Locate and identify every blood parasite.
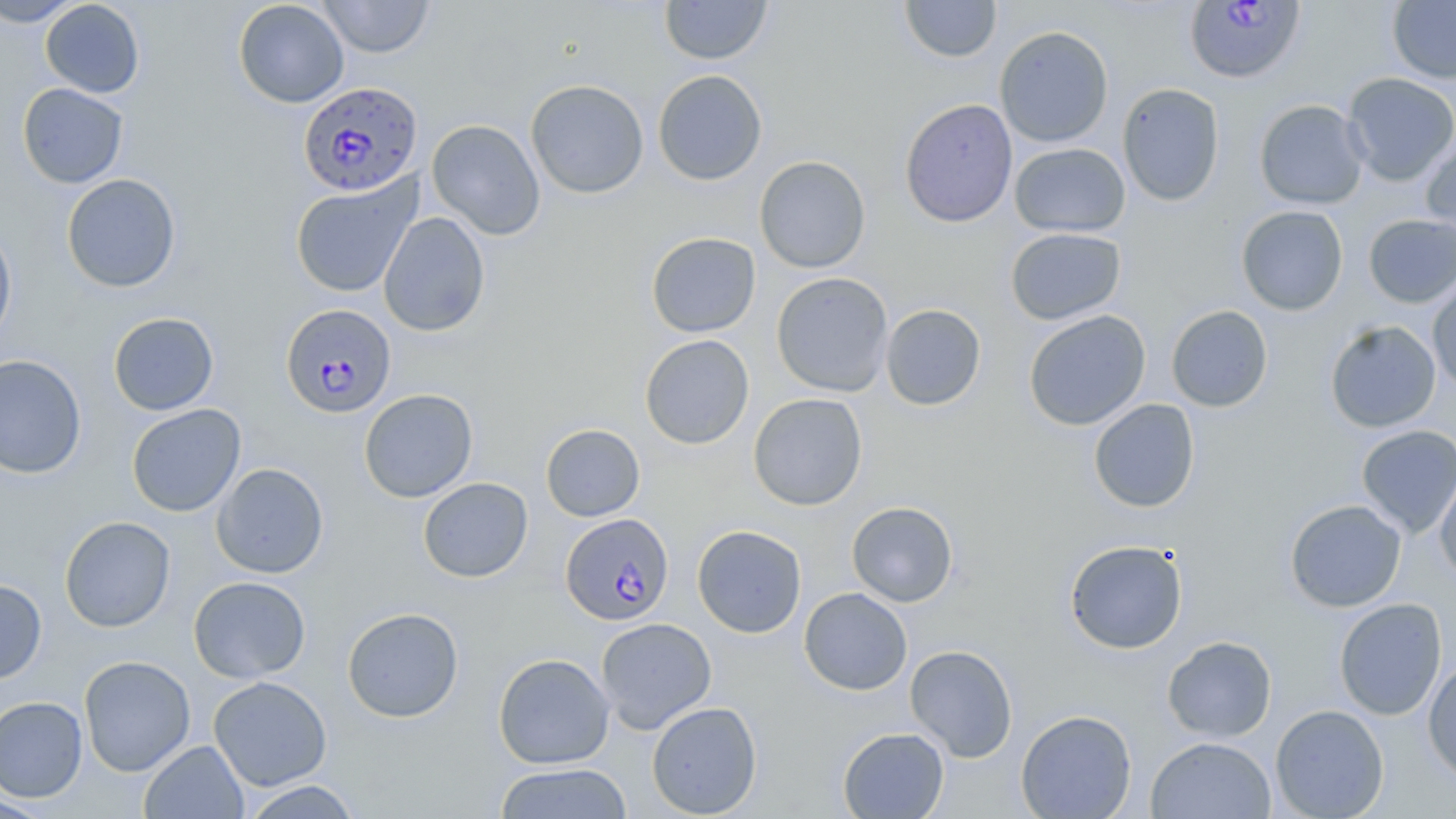

Approximate bounding boxes as (x1,y1)-(x2,y2) corner pairs in pixels.
Plasmodium falciparum-infected red blood cells: (1184,0)-(1305,84), (298,81)-(423,196), (282,303)-(398,418), (560,513)-(674,626).
No Plasmodium ovale, Plasmodium malariae, Plasmodium vivax, Babesia divergens, or Trypanosoma brucei observed.

{
  "slide_level_diagnosis": "Plasmodium falciparum",
  "preparation": "thin blood smear",
  "modality": "light microscopy",
  "magnification": "1000x",
  "image_size": "1456×819 pixels",
  "field_of_view": "single",
  "uninfected_red_blood_cell_locations": "approximate bounding boxes as (x1,y1)-(x2,y2) corner pairs in pixels: (0,0)-(83,27), (40,0)-(145,98), (233,0)-(349,108), (317,0)-(434,58), (660,0)-(772,65), (900,1)-(1001,63), (1388,1)-(1456,84), (995,26)-(1114,147), (652,69)-(768,186), (1341,72)-(1456,186), (525,79)-(649,198), (1117,82)-(1225,207), (17,83)-(128,188), (900,98)-(1018,228), (1254,99)-(1369,209), (427,119)-(545,240), (1421,135)-(1456,246), (1010,143)-(1130,237), (755,155)-(871,274), (61,173)-(181,293), (290,176)-(421,297), (1236,205)-(1348,315), (378,212)-(490,337), (1363,214)-(1456,308), (0,221)-(17,350), (1005,227)-(1126,325), (646,232)-(761,337), (771,272)-(894,397), (1427,276)-(1456,393), (880,304)-(986,411), (1166,305)-(1273,412), (1023,310)-(1151,431), (108,312)-(219,416), (1325,320)-(1441,433), (639,334)-(754,450), (0,354)-(87,479), (359,389)-(478,503), (747,393)-(868,511), (1088,398)-(1200,513), (126,403)-(246,517), (541,424)-(645,521), (1356,425)-(1456,538), (211,463)-(329,578), (1434,464)-(1456,582), (418,477)-(533,582), (1285,499)-(1407,612), (847,501)-(958,607), (59,516)-(176,632), (691,524)-(807,638), (1064,539)-(1188,654), (188,576)-(311,683), (0,579)-(47,683), (799,587)-(912,695), (1334,598)-(1448,721), (342,607)-(464,722), (595,617)-(716,734), (1162,635)-(1277,742), (904,645)-(1018,762), (493,652)-(615,769), (78,655)-(196,776), (1423,656)-(1456,787), (208,676)-(332,791), (0,696)-(88,802), (646,701)-(762,817), (1270,704)-(1389,819), (1015,709)-(1137,818), (837,727)-(949,818), (1145,737)-(1277,819), (140,740)-(249,819), (494,763)-(633,819), (240,780)-(364,818), (0,795)-(55,818)",
  "stain": "May-Grünwald-Giemsa"
}